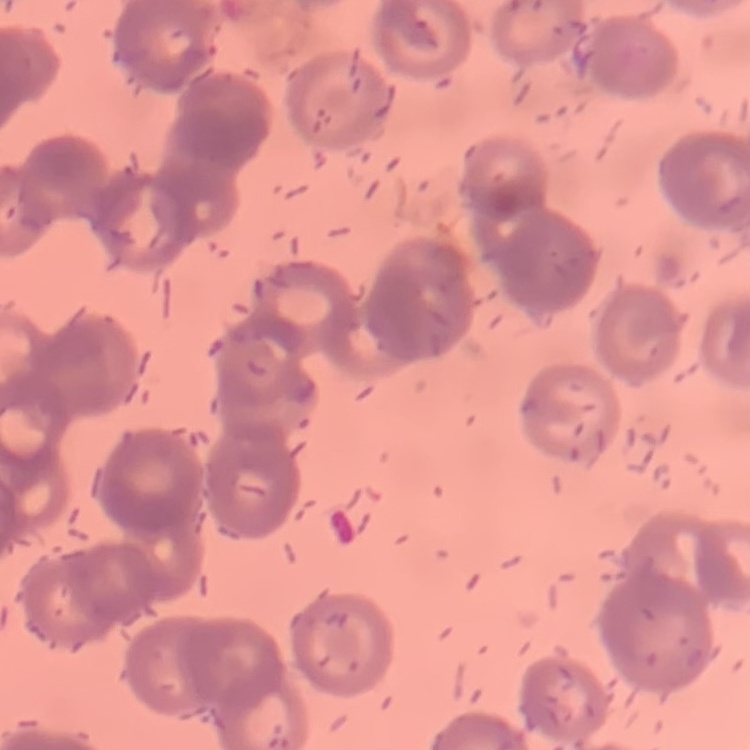
Summary:
  - Red blood cell morphology: rouleaux formation
  - Image type: square crop of a larger photomicrograph
  - Preparation: thin blood film
  - Stain: Field's or Giemsa